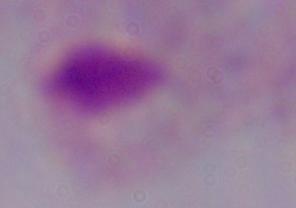
A trichomonad is shown. 1000x magnification. Photomicrograph.